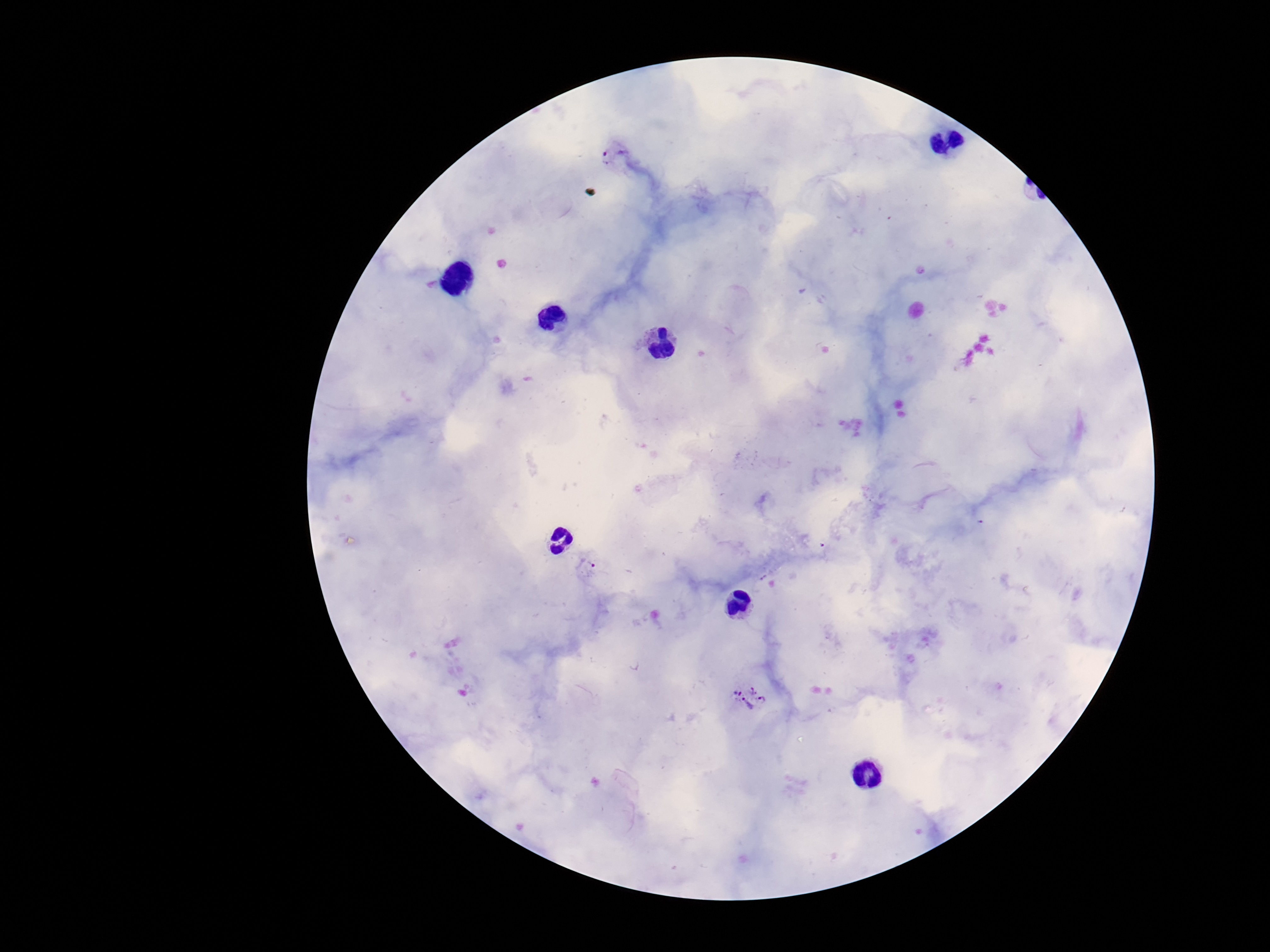
Approximate object centers, in pixels from the top-left corner.
Summary:
  - Plasmodium parasite locations: (x=608, y=156), (x=586, y=565), (x=751, y=699)
  - Preparation: thick blood film
  - Patient malaria status: infected
  - Capture: smartphone camera through the microscope eyepiece
  - Image size: 1270×952 pixels
  - Field of view: single
  - Magnification: 100x
  - Stain: Giemsa